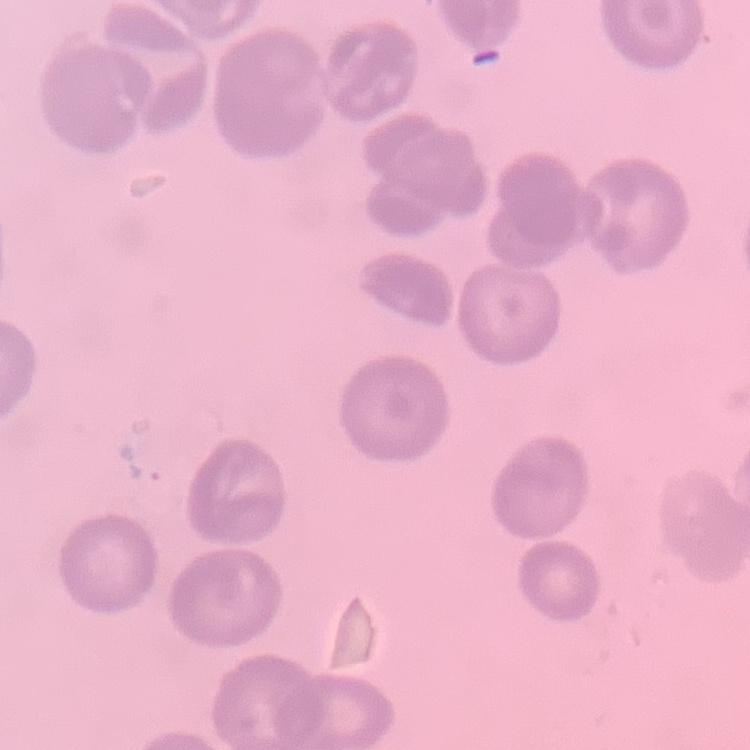
The red blood cells show no rouleaux formation. Square crop of a larger photomicrograph. Stained with either Field's or Giemsa. Thin blood smear.